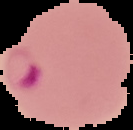
Summary:
  - Preparation: thin blood smear
  - Image size: 133×130 pixels
  - Image type: cell region segmented out of the field of view; surrounding area masked to black
  - Malaria status: parasitized